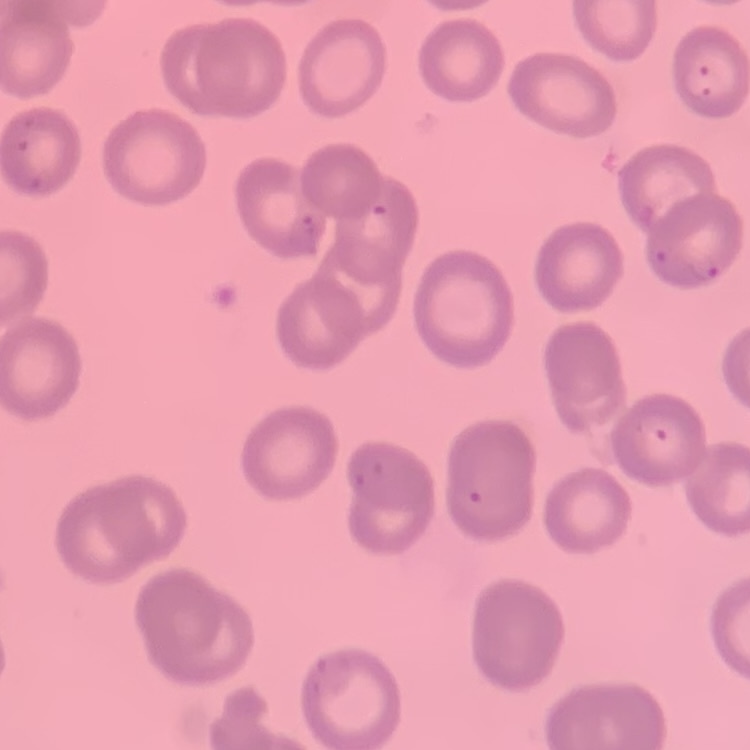

red blood cell morphology = no rouleaux formation
stain = Field's or Giemsa
image type = one tile cut from a larger photomicrograph
preparation = thin blood film